Locate every white blood cell.
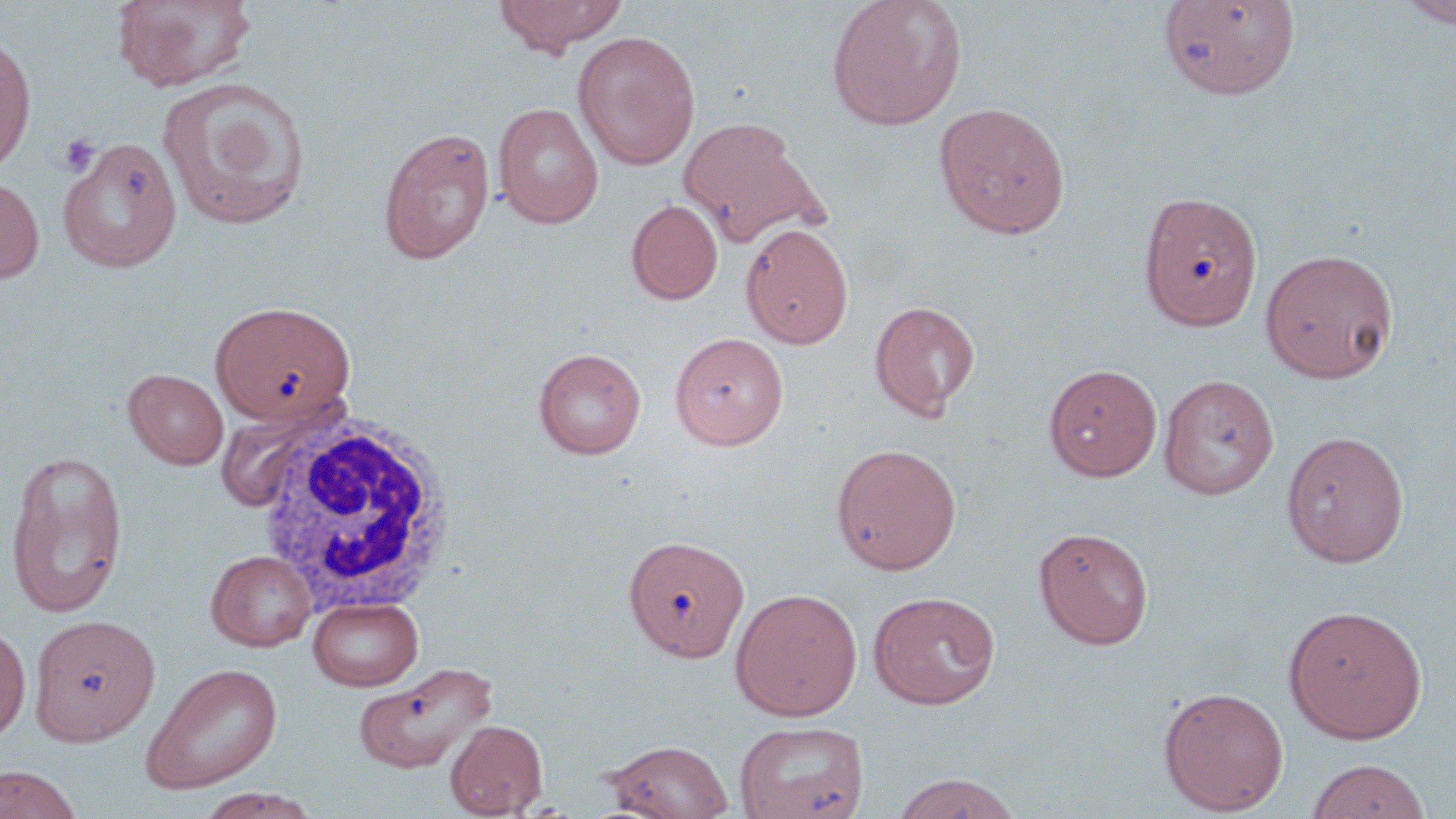

Approximate bounding boxes as (x1,y1)-(x2,y2) corner pairs in pixels.
White blood cells: (252,412)-(458,613).

Summary:
  - Uninfected red blood cell locations: (112,0)-(256,92), (493,0)-(627,54), (826,0)-(967,130), (1397,0)-(1456,29), (1157,1)-(1301,100), (572,30)-(701,169), (0,36)-(36,174), (158,77)-(311,229), (933,101)-(1071,238), (493,102)-(604,229), (678,115)-(827,247), (377,126)-(496,264), (58,138)-(182,273), (0,175)-(44,285), (1137,189)-(1263,331), (626,199)-(723,304), (740,222)-(854,349), (1259,247)-(1399,384), (210,300)-(356,425), (868,300)-(981,420), (669,332)-(788,450), (533,347)-(646,459), (1043,363)-(1163,481), (124,369)-(229,469), (1159,374)-(1279,499), (1281,430)-(1410,567), (830,442)-(962,574), (3,448)-(130,619), (1033,527)-(1155,649), (624,534)-(749,662), (206,550)-(316,650), (730,587)-(863,721), (867,590)-(1001,709), (308,596)-(423,691), (1283,604)-(1428,743), (29,613)-(160,745), (0,624)-(31,741), (354,660)-(498,774), (141,662)-(283,793), (1157,686)-(1289,815), (446,719)-(548,818), (734,720)-(870,819), (603,739)-(734,818), (1306,758)-(1431,819), (0,765)-(84,818), (891,773)-(1022,818), (194,788)-(322,819)
  - Platelet locations: (59,134)-(100,175)
  - Slide-level diagnosis: no evidence of blood parasites
  - Magnification: 1000x
  - Field of view: single
  - Modality: optical microscopy
  - Stain: May-Grünwald-Giemsa
  - Image size: 1456×819 pixels
  - Preparation: thin blood smear